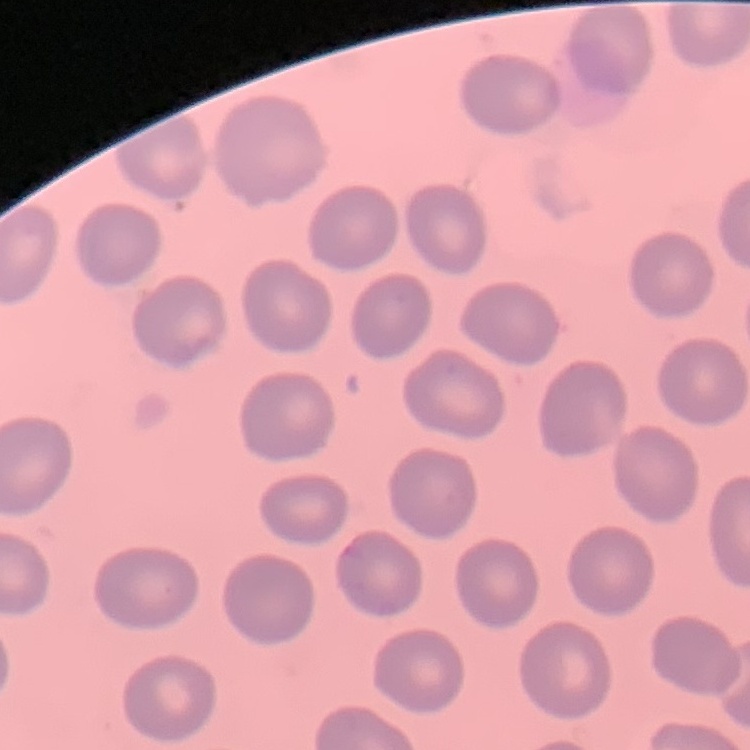

The red blood cells exhibit no rouleaux formation. Thin blood smear. Field's or Giemsa stain. Square crop of a larger photomicrograph.